Identify the blood parasite species.
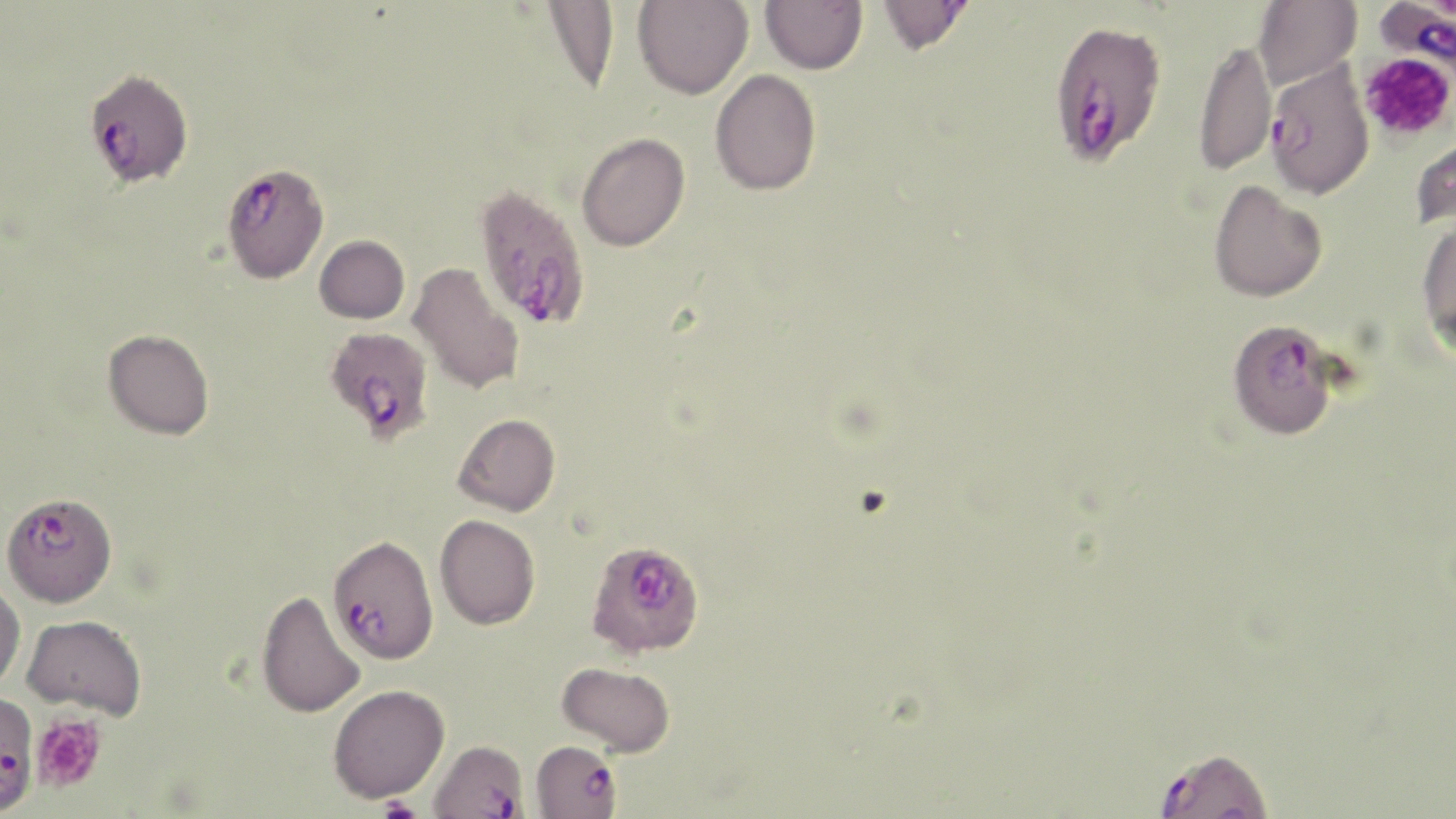
Plasmodium falciparum.

Summary:
  - Coordinate format: approximate bounding boxes as [x1, y1, x2, y2] in pixels
  - Uninfected red blood cell locations: [633, 0, 753, 99], [760, 0, 867, 74], [877, 0, 975, 55], [1253, 0, 1361, 89], [541, 1, 619, 95], [1193, 38, 1277, 176], [709, 69, 822, 196], [1409, 124, 1456, 233], [576, 132, 690, 251], [1209, 180, 1327, 302], [1416, 218, 1456, 354], [314, 235, 409, 323], [408, 262, 525, 395], [103, 328, 214, 439], [453, 413, 561, 516], [435, 514, 540, 629], [0, 582, 25, 692], [256, 590, 366, 719], [23, 615, 147, 719], [557, 661, 676, 757], [328, 684, 450, 803]
  - Platelet locations: [1359, 52, 1455, 143], [30, 714, 106, 794], [373, 798, 426, 819]
  - Plasmodium falciparum-infected red blood cell locations: [1375, 0, 1456, 74], [1048, 18, 1167, 166], [1265, 58, 1374, 199], [87, 69, 200, 191], [222, 163, 329, 284], [474, 183, 591, 330], [1228, 318, 1341, 439], [310, 328, 430, 451], [5, 495, 117, 612], [332, 537, 444, 666], [585, 539, 704, 658], [0, 693, 39, 815], [428, 738, 529, 818], [530, 739, 623, 818], [1152, 745, 1275, 819]
  - Image size: 1456×819 pixels
  - Modality: optical microscopy
  - Preparation: thin blood film
  - Stain: May-Grünwald-Giemsa
  - Magnification: 1000x
  - Field of view: single